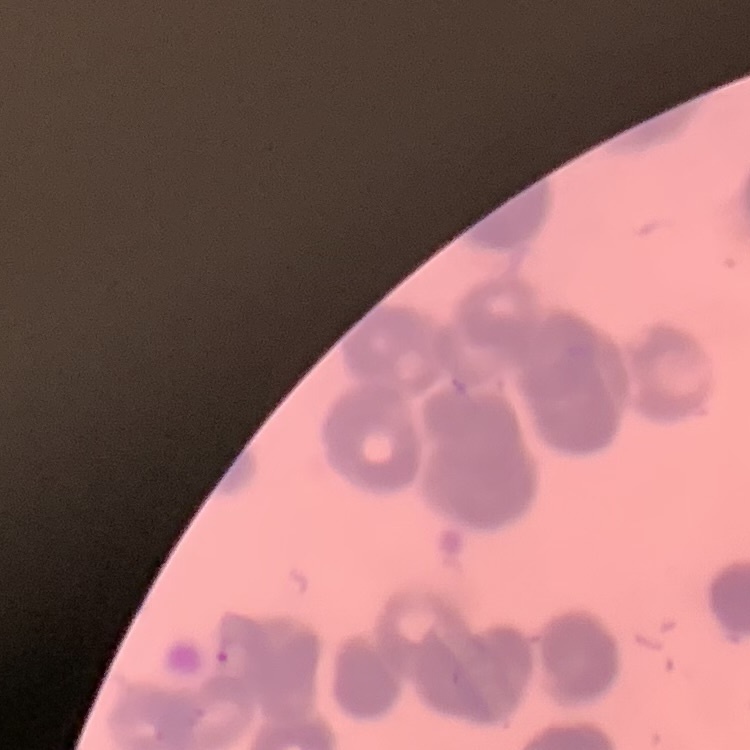
The erythrocytes show rouleaux formation. Thin peripheral smear. One tile cut from a larger photomicrograph. Field's or Giemsa stain.